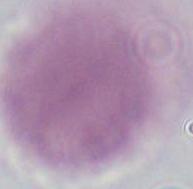
Summary:
  - Modality: micrograph
  - Magnification: 1000x
  - Identification: erythrocyte